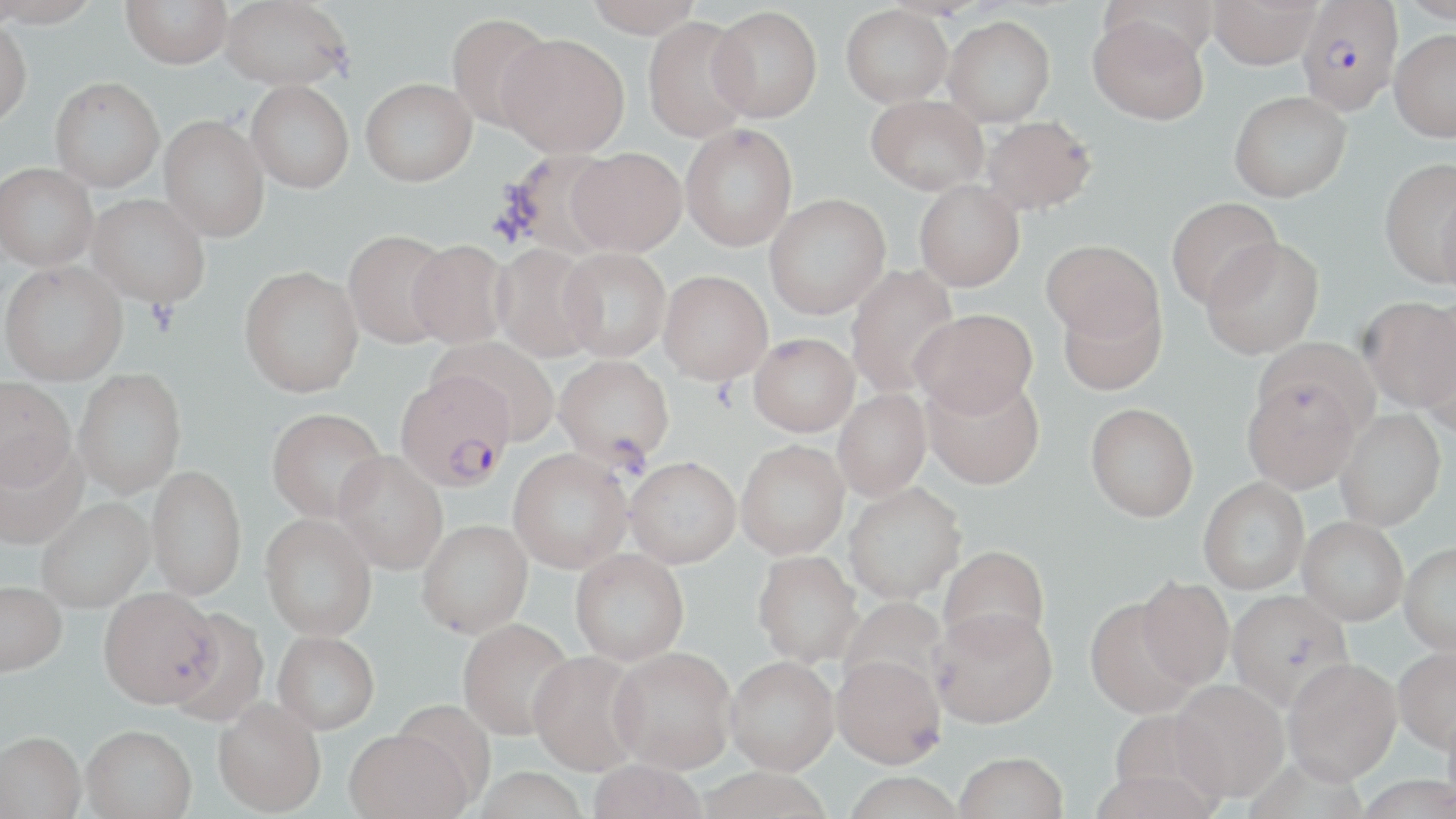
Summary:
  - Coordinate format: approximate bounding boxes as (x1,y1)-(x2,y2) corner pairs in pixels
  - Platelet locations: (146,301)-(179,336), (710,380)-(740,413)
  - Plasmodium falciparum-infected red blood cell locations: (1297,0)-(1403,115), (396,374)-(516,496)
  - Uninfected red blood cell locations: (0,0)-(101,28), (121,0)-(232,68), (585,0)-(703,37), (1207,0)-(1322,69), (220,1)-(353,89), (1396,1)-(1456,25), (841,5)-(952,107), (708,6)-(822,122), (445,13)-(557,133), (1088,14)-(1209,125), (642,16)-(755,142), (943,16)-(1055,126), (0,18)-(32,129), (1390,29)-(1456,142), (498,34)-(630,157), (49,76)-(164,192), (360,78)-(477,186), (246,80)-(354,193), (1229,91)-(1351,202), (866,95)-(988,194), (159,115)-(269,241), (981,116)-(1096,215), (680,123)-(798,251), (567,147)-(687,255), (496,148)-(620,262), (1380,158)-(1456,287), (0,162)-(98,271), (914,180)-(1024,291), (1434,180)-(1456,298), (87,194)-(209,308), (764,194)-(890,318), (1167,197)-(1283,309), (343,229)-(455,350), (1202,236)-(1324,360), (407,239)-(510,349), (1041,240)-(1164,345), (491,244)-(601,364), (559,248)-(671,362), (0,262)-(128,387), (846,264)-(960,398), (239,266)-(364,398), (658,271)-(772,387), (1057,294)-(1167,396), (1358,298)-(1456,412), (911,309)-(1038,418), (1417,319)-(1456,438), (748,335)-(859,439), (430,337)-(559,445), (553,358)-(674,472), (74,371)-(187,500), (922,374)-(1045,491), (1242,374)-(1361,495), (0,380)-(75,493), (834,390)-(932,502), (1085,404)-(1198,523), (266,410)-(386,526), (1335,411)-(1446,532), (0,440)-(89,552), (736,444)-(849,563), (508,454)-(632,577), (334,455)-(447,577), (625,461)-(742,572), (146,468)-(246,603), (1198,478)-(1309,595), (844,485)-(966,606), (37,500)-(155,614), (259,516)-(377,644), (1296,519)-(1407,628), (417,523)-(533,642), (938,546)-(1050,656), (1399,546)-(1456,659), (570,551)-(689,668), (752,553)-(863,670), (1135,578)-(1234,690), (0,586)-(67,682), (99,592)-(220,713), (1226,592)-(1354,715), (1085,599)-(1200,721), (930,609)-(1058,732), (165,611)-(269,728), (458,622)-(575,744), (274,635)-(379,737), (609,651)-(737,778), (1393,651)-(1456,757), (528,652)-(646,778), (831,660)-(946,773), (724,661)-(839,780), (1283,662)-(1403,788), (1170,680)-(1290,804), (213,702)-(326,818), (81,730)-(197,818), (344,732)-(472,819), (0,736)-(86,819), (953,756)-(1069,819), (588,762)-(707,819), (695,771)-(832,819), (473,772)-(586,819), (841,777)-(965,819), (1354,778)-(1456,818)
  - Slide-level diagnosis: Plasmodium falciparum
  - Stain: May-Grünwald-Giemsa
  - Image size: 1456×819 pixels
  - Modality: optical microscopy
  - Magnification: 1000x
  - Preparation: thin blood smear
  - Field of view: single